Identify the parasite.
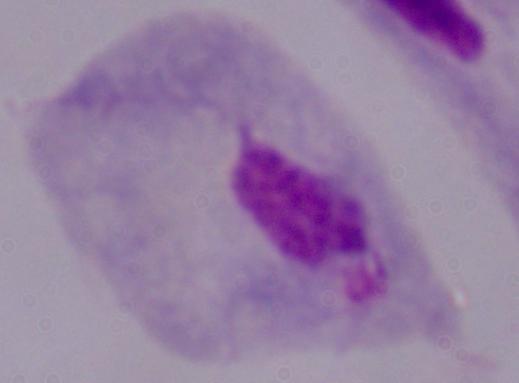

A trichomonad.

Summary:
  - Magnification: 1000x
  - Modality: micrograph